Describe the morphology of the erythrocytes.
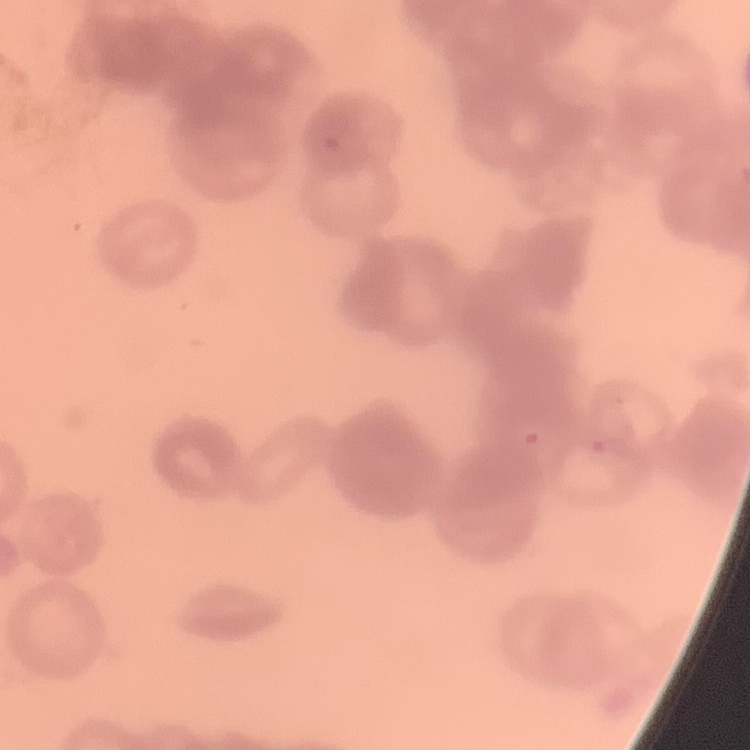

Rouleaux formation.

image type = one tile cut from a larger photomicrograph
stain = Field's or Giemsa
preparation = thin blood film